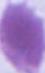
Summary:
  - Identification: erythrocyte
  - Magnification: 1000x
  - Modality: micrograph